Outline each Plasmodium falciparum-infected red blood cell.
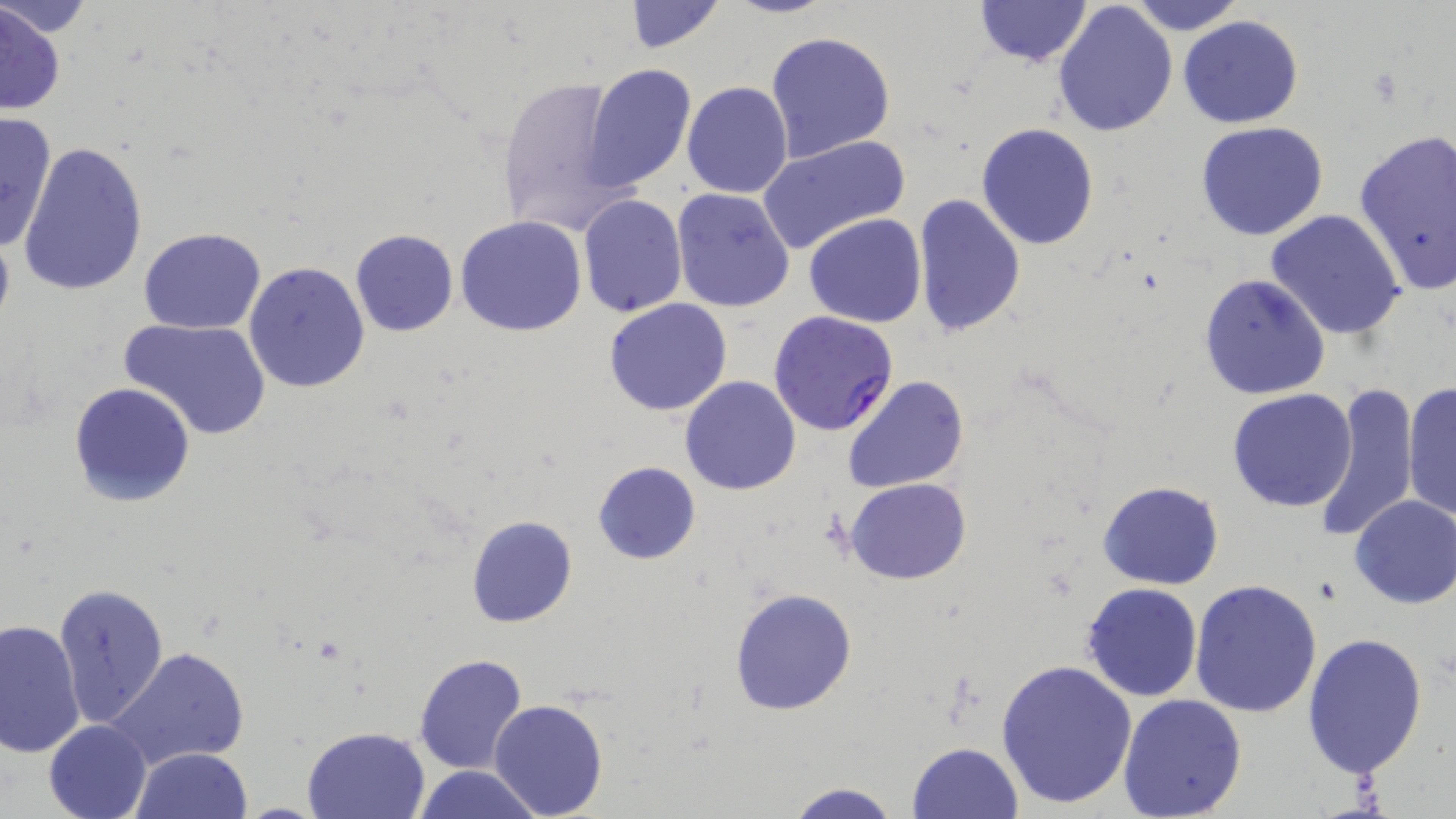
Approximate bounding boxes as named x1/y1/x2/y2 corners in pixels.
Plasmodium falciparum-infected red blood cells: (x1=767, y1=309, x2=899, y2=436).

Uninfected red blood cell locations: (x1=0, y1=0, x2=98, y2=38), (x1=621, y1=0, x2=726, y2=54), (x1=722, y1=0, x2=835, y2=19), (x1=1126, y1=0, x2=1245, y2=35), (x1=973, y1=1, x2=1093, y2=69), (x1=1053, y1=1, x2=1178, y2=139), (x1=1, y1=4, x2=68, y2=117), (x1=1178, y1=16, x2=1305, y2=129), (x1=766, y1=30, x2=896, y2=162), (x1=583, y1=63, x2=699, y2=190), (x1=495, y1=73, x2=635, y2=240), (x1=681, y1=82, x2=793, y2=199), (x1=0, y1=110, x2=58, y2=255), (x1=1194, y1=121, x2=1330, y2=241), (x1=976, y1=123, x2=1102, y2=250), (x1=1352, y1=128, x2=1456, y2=295), (x1=757, y1=134, x2=911, y2=254), (x1=15, y1=140, x2=149, y2=298), (x1=671, y1=189, x2=795, y2=313), (x1=577, y1=193, x2=688, y2=317), (x1=912, y1=193, x2=1027, y2=338), (x1=1265, y1=208, x2=1406, y2=340), (x1=805, y1=213, x2=927, y2=327), (x1=455, y1=216, x2=587, y2=337), (x1=139, y1=227, x2=266, y2=335), (x1=350, y1=228, x2=458, y2=336), (x1=243, y1=261, x2=370, y2=394), (x1=1197, y1=272, x2=1331, y2=400), (x1=603, y1=299, x2=733, y2=417), (x1=118, y1=317, x2=272, y2=440), (x1=680, y1=375, x2=801, y2=495), (x1=841, y1=375, x2=968, y2=494), (x1=1403, y1=381, x2=1456, y2=524), (x1=68, y1=382, x2=197, y2=506), (x1=1314, y1=382, x2=1419, y2=542), (x1=1228, y1=387, x2=1360, y2=512), (x1=593, y1=461, x2=700, y2=566), (x1=845, y1=478, x2=971, y2=585), (x1=1097, y1=481, x2=1224, y2=589), (x1=1348, y1=495, x2=1456, y2=609), (x1=466, y1=515, x2=578, y2=627), (x1=1189, y1=578, x2=1323, y2=719), (x1=53, y1=582, x2=168, y2=726), (x1=1080, y1=583, x2=1202, y2=701), (x1=729, y1=588, x2=858, y2=714), (x1=0, y1=617, x2=86, y2=761), (x1=1302, y1=633, x2=1430, y2=779), (x1=107, y1=645, x2=251, y2=773), (x1=413, y1=652, x2=528, y2=776), (x1=995, y1=658, x2=1138, y2=807), (x1=1117, y1=693, x2=1247, y2=819), (x1=487, y1=698, x2=609, y2=818), (x1=43, y1=719, x2=151, y2=819), (x1=302, y1=726, x2=430, y2=819), (x1=905, y1=742, x2=1023, y2=819), (x1=131, y1=747, x2=254, y2=819), (x1=412, y1=764, x2=544, y2=819), (x1=778, y1=781, x2=905, y2=819). Slide-level diagnosis: Plasmodium falciparum. Thin blood film. Image is 1456×819 pixels. May-Grünwald-Giemsa stain. Optical microscopy. 1000x magnification. One field of a larger specimen.